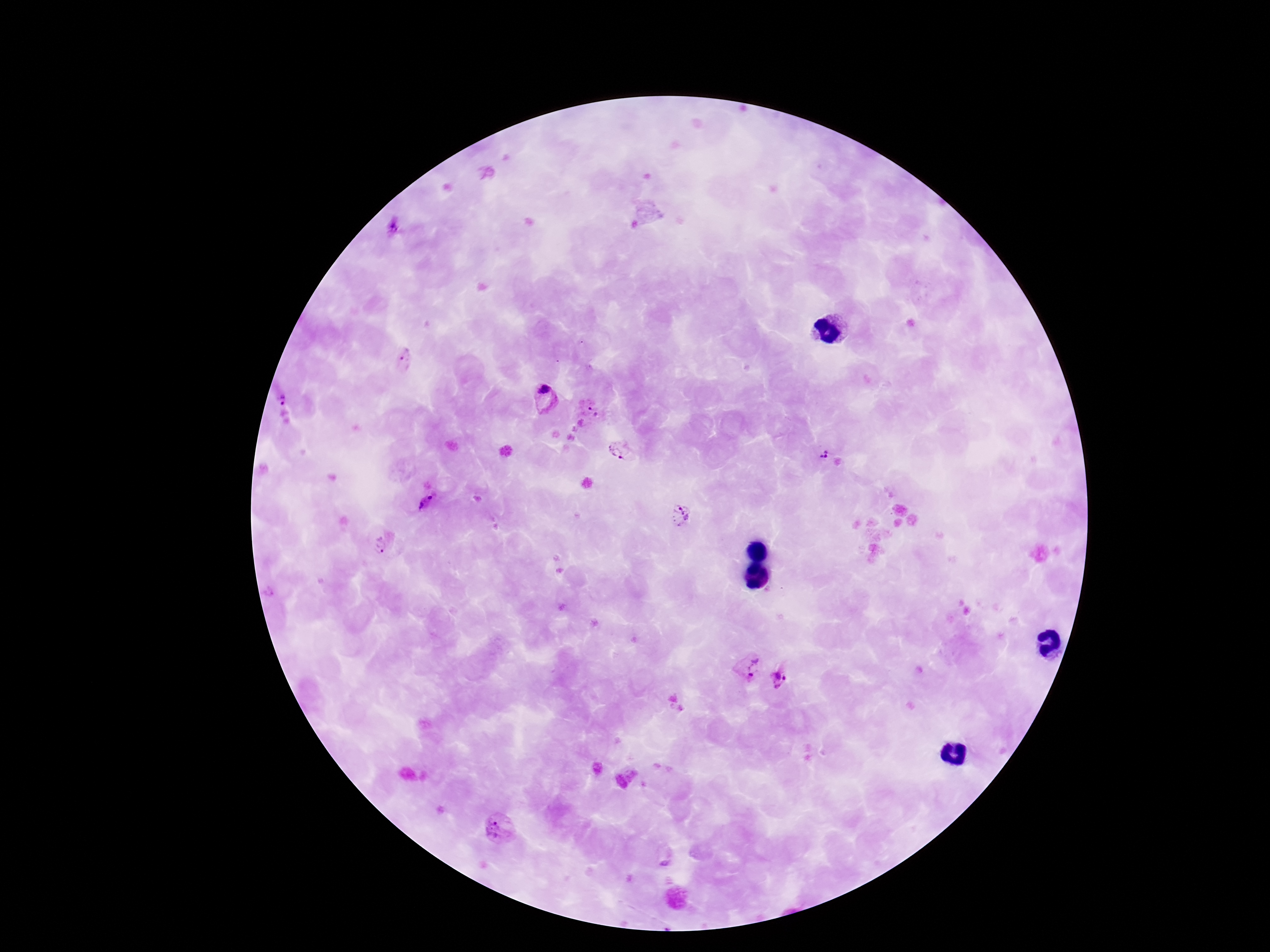
Approximate centers as {x, y} in pixels. Plasmodium parasite locations: {392, 228}, {406, 360}, {281, 396}, {542, 399}, {594, 411}, {619, 449}, {819, 456}, {426, 503}, {680, 516}, {380, 545}, {746, 667}, {781, 677}, {494, 829}. Giemsa-stained preparation. Thick blood film. Patient malaria status: infected. Photographed through the microscope eyepiece with a smartphone camera. Image is 1270×952 pixels. Single field of view. 100x magnification.